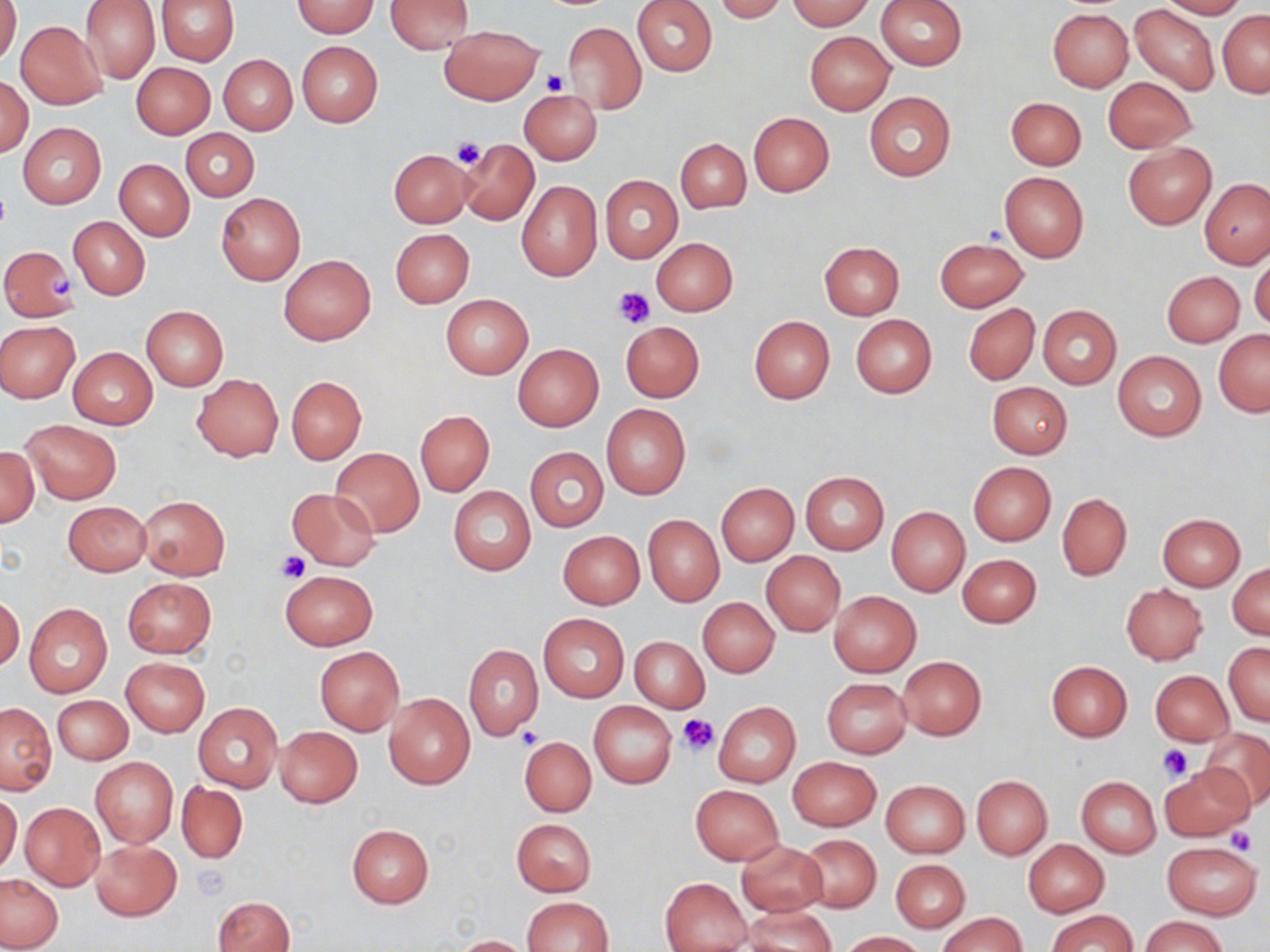

Approximate bounding boxes as named x1/y1/x2/y2 corners in pixels. Uninfected red blood cell locations: (x1=0, y1=0, x2=21, y2=68), (x1=79, y1=0, x2=160, y2=85), (x1=156, y1=0, x2=240, y2=65), (x1=386, y1=0, x2=474, y2=54), (x1=632, y1=0, x2=717, y2=76), (x1=714, y1=0, x2=789, y2=22), (x1=785, y1=0, x2=875, y2=31), (x1=876, y1=0, x2=966, y2=70), (x1=1157, y1=0, x2=1246, y2=19), (x1=293, y1=1, x2=377, y2=37), (x1=83, y1=2, x2=236, y2=74), (x1=1130, y1=5, x2=1219, y2=97), (x1=1047, y1=9, x2=1133, y2=91), (x1=1217, y1=10, x2=1269, y2=98), (x1=16, y1=21, x2=107, y2=109), (x1=563, y1=21, x2=645, y2=114), (x1=441, y1=25, x2=543, y2=103), (x1=804, y1=31, x2=895, y2=114), (x1=297, y1=41, x2=382, y2=128), (x1=219, y1=55, x2=297, y2=134), (x1=131, y1=62, x2=215, y2=138), (x1=1, y1=74, x2=33, y2=158), (x1=1103, y1=77, x2=1195, y2=152), (x1=519, y1=89, x2=602, y2=164), (x1=863, y1=91, x2=955, y2=182), (x1=1006, y1=96, x2=1086, y2=169), (x1=748, y1=112, x2=834, y2=197), (x1=18, y1=122, x2=106, y2=208), (x1=182, y1=128, x2=259, y2=200), (x1=456, y1=138, x2=539, y2=226), (x1=676, y1=138, x2=750, y2=214), (x1=1123, y1=144, x2=1216, y2=229), (x1=389, y1=149, x2=474, y2=227), (x1=115, y1=158, x2=194, y2=240), (x1=999, y1=171, x2=1090, y2=262), (x1=599, y1=174, x2=683, y2=263), (x1=1201, y1=179, x2=1269, y2=268), (x1=516, y1=181, x2=602, y2=281), (x1=216, y1=193, x2=305, y2=285), (x1=68, y1=216, x2=151, y2=299), (x1=391, y1=228, x2=475, y2=308), (x1=652, y1=237, x2=737, y2=315), (x1=935, y1=238, x2=1028, y2=311), (x1=818, y1=241, x2=904, y2=319), (x1=1, y1=245, x2=78, y2=321), (x1=1249, y1=250, x2=1270, y2=332), (x1=278, y1=255, x2=376, y2=345), (x1=1163, y1=271, x2=1244, y2=346), (x1=440, y1=294, x2=533, y2=379), (x1=963, y1=303, x2=1039, y2=385), (x1=141, y1=305, x2=229, y2=391), (x1=1038, y1=305, x2=1121, y2=388), (x1=850, y1=313, x2=937, y2=397), (x1=749, y1=315, x2=835, y2=404), (x1=621, y1=320, x2=705, y2=403), (x1=0, y1=321, x2=80, y2=403), (x1=1214, y1=329, x2=1270, y2=416), (x1=513, y1=343, x2=604, y2=431), (x1=67, y1=346, x2=157, y2=428), (x1=1113, y1=350, x2=1206, y2=440), (x1=191, y1=373, x2=283, y2=460), (x1=286, y1=375, x2=367, y2=464), (x1=985, y1=380, x2=1073, y2=458), (x1=600, y1=402, x2=692, y2=499), (x1=415, y1=410, x2=495, y2=496), (x1=19, y1=420, x2=121, y2=504), (x1=0, y1=447, x2=39, y2=526), (x1=526, y1=447, x2=608, y2=532), (x1=331, y1=448, x2=424, y2=537), (x1=968, y1=461, x2=1056, y2=545), (x1=800, y1=471, x2=889, y2=553), (x1=717, y1=483, x2=798, y2=565), (x1=448, y1=486, x2=536, y2=576), (x1=287, y1=487, x2=381, y2=569), (x1=1056, y1=493, x2=1132, y2=580), (x1=137, y1=495, x2=231, y2=580), (x1=62, y1=501, x2=151, y2=576), (x1=886, y1=506, x2=970, y2=596), (x1=1158, y1=513, x2=1245, y2=589), (x1=643, y1=514, x2=724, y2=607), (x1=558, y1=529, x2=645, y2=610), (x1=760, y1=551, x2=845, y2=636), (x1=957, y1=553, x2=1042, y2=628), (x1=1229, y1=563, x2=1269, y2=639), (x1=280, y1=570, x2=378, y2=649), (x1=122, y1=577, x2=216, y2=658), (x1=1121, y1=584, x2=1207, y2=664), (x1=829, y1=591, x2=921, y2=676), (x1=1, y1=594, x2=24, y2=672), (x1=697, y1=597, x2=779, y2=677), (x1=24, y1=603, x2=112, y2=698), (x1=537, y1=612, x2=629, y2=702), (x1=629, y1=635, x2=709, y2=713), (x1=1224, y1=642, x2=1269, y2=726), (x1=463, y1=644, x2=543, y2=741), (x1=314, y1=647, x2=403, y2=735), (x1=898, y1=656, x2=987, y2=739), (x1=122, y1=658, x2=208, y2=736), (x1=1046, y1=661, x2=1132, y2=740), (x1=1150, y1=670, x2=1233, y2=745), (x1=822, y1=677, x2=912, y2=759), (x1=384, y1=693, x2=475, y2=790), (x1=52, y1=694, x2=133, y2=765), (x1=1, y1=702, x2=56, y2=794), (x1=194, y1=702, x2=281, y2=792), (x1=589, y1=702, x2=677, y2=788), (x1=715, y1=703, x2=800, y2=786), (x1=275, y1=725, x2=362, y2=807), (x1=1201, y1=727, x2=1270, y2=809), (x1=520, y1=736, x2=596, y2=816), (x1=90, y1=756, x2=178, y2=848), (x1=788, y1=756, x2=880, y2=830), (x1=1160, y1=764, x2=1256, y2=841), (x1=971, y1=775, x2=1052, y2=858), (x1=1076, y1=776, x2=1161, y2=857), (x1=880, y1=779, x2=970, y2=857), (x1=177, y1=782, x2=248, y2=863), (x1=689, y1=784, x2=784, y2=865), (x1=0, y1=794, x2=21, y2=876), (x1=21, y1=803, x2=105, y2=890), (x1=511, y1=818, x2=597, y2=896), (x1=346, y1=823, x2=435, y2=908), (x1=799, y1=834, x2=881, y2=912), (x1=735, y1=839, x2=828, y2=917), (x1=1023, y1=839, x2=1109, y2=916), (x1=91, y1=840, x2=181, y2=920), (x1=1162, y1=842, x2=1261, y2=919), (x1=890, y1=858, x2=971, y2=932), (x1=0, y1=873, x2=64, y2=951), (x1=660, y1=878, x2=751, y2=952), (x1=214, y1=895, x2=294, y2=952), (x1=521, y1=896, x2=613, y2=952), (x1=744, y1=906, x2=836, y2=952), (x1=1047, y1=909, x2=1137, y2=952), (x1=938, y1=912, x2=1026, y2=952), (x1=1139, y1=915, x2=1230, y2=952), (x1=837, y1=931, x2=928, y2=951), (x1=453, y1=935, x2=534, y2=952). Platelet locations: (x1=541, y1=69, x2=570, y2=96), (x1=451, y1=139, x2=487, y2=169), (x1=49, y1=272, x2=76, y2=303), (x1=613, y1=288, x2=654, y2=329), (x1=278, y1=551, x2=309, y2=582), (x1=677, y1=713, x2=720, y2=757), (x1=517, y1=728, x2=541, y2=749), (x1=1158, y1=743, x2=1194, y2=783), (x1=1227, y1=827, x2=1258, y2=858), (x1=193, y1=863, x2=231, y2=902). Slide-level diagnosis: negative for blood parasites. May-Grünwald-Giemsa-stained preparation. Captured at 1000x magnification. Thin blood smear. Optical microscopy. One field of a larger specimen. Image is 1270×952 pixels.